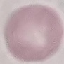

{
  "malaria_status": "uninfected",
  "preparation": "thin blood film",
  "capture": "smartphone camera at the microscope eyepiece",
  "stain": "Giemsa",
  "image_type": "cell patch, automatically extracted from a larger field of view and resized to 64 × 64 pixels"
}